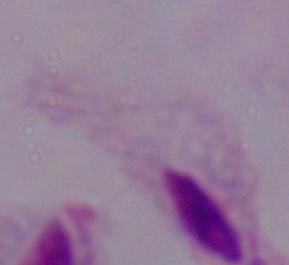
Captured at 1000x magnification. Photomicrograph. A trichomonad is seen.